Assess this cell for malaria.
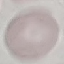

It is uninfected.

Summary:
  - Preparation: thin blood smear
  - Image type: cell patch, automatically extracted from a larger field of view and resized to 64 × 64 pixels
  - Capture: smartphone camera at the microscope eyepiece
  - Stain: Giemsa